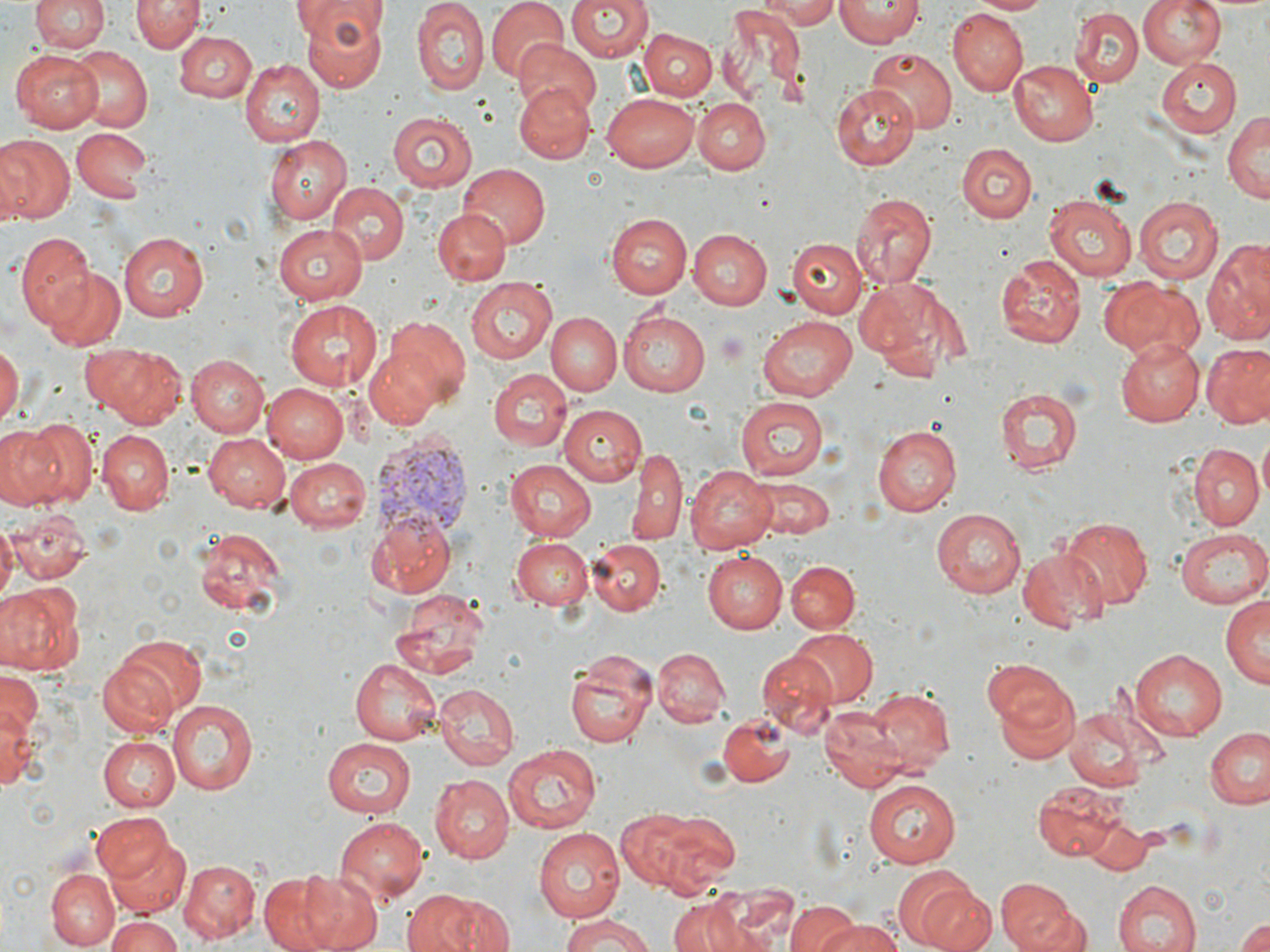

Approximate bounding boxes as (x1, y1, x2, y2) in pixels. Uninfected red blood cell locations: (31, 0, 108, 54), (133, 0, 203, 53), (294, 0, 390, 89), (487, 0, 569, 83), (566, 0, 654, 61), (756, 0, 844, 26), (835, 0, 922, 46), (967, 0, 1052, 15), (1138, 0, 1226, 68), (413, 1, 488, 96), (719, 4, 806, 99), (949, 10, 1028, 96), (1071, 10, 1142, 85), (639, 28, 717, 101), (173, 30, 257, 103), (515, 41, 604, 118), (65, 44, 153, 132), (866, 47, 957, 134), (11, 48, 105, 131), (1156, 57, 1243, 139), (238, 58, 323, 146), (1008, 58, 1097, 146), (514, 81, 595, 163), (833, 88, 918, 170), (604, 91, 702, 171), (696, 96, 771, 173), (1223, 111, 1269, 206), (388, 112, 475, 192), (71, 127, 152, 201), (0, 135, 73, 226), (264, 135, 352, 225), (959, 143, 1033, 222), (458, 164, 549, 247), (327, 181, 408, 266), (849, 192, 939, 289), (1042, 193, 1137, 283), (1133, 195, 1224, 284), (288, 197, 398, 288), (432, 209, 510, 284), (605, 213, 690, 297), (271, 222, 368, 304), (688, 229, 772, 309), (15, 232, 96, 328), (119, 232, 209, 320), (791, 237, 866, 317), (1204, 240, 1270, 345), (996, 253, 1085, 350), (44, 268, 126, 353), (465, 278, 556, 364), (860, 279, 958, 379), (1100, 280, 1203, 361), (283, 299, 384, 390), (619, 308, 714, 395), (547, 313, 619, 395), (757, 315, 861, 402), (384, 316, 470, 402), (1117, 341, 1204, 426), (1203, 342, 1270, 427), (84, 344, 187, 427), (0, 345, 21, 426), (365, 346, 444, 429), (187, 355, 269, 435), (488, 367, 571, 451), (264, 383, 349, 463), (996, 386, 1083, 477), (739, 396, 831, 478), (558, 404, 646, 486), (24, 417, 98, 508), (1, 425, 66, 510), (871, 425, 961, 516), (95, 428, 175, 515), (202, 432, 290, 511), (1188, 443, 1263, 529), (629, 446, 687, 546), (285, 458, 371, 532), (504, 459, 598, 539), (683, 464, 777, 553), (753, 480, 835, 538), (932, 508, 1026, 598), (6, 510, 90, 584), (370, 512, 458, 597), (1058, 517, 1153, 611), (0, 522, 16, 608), (1177, 526, 1270, 608), (194, 529, 288, 618), (510, 535, 593, 611), (588, 539, 666, 615), (1017, 550, 1108, 631), (705, 551, 788, 633), (786, 559, 859, 634), (0, 582, 83, 676), (391, 588, 489, 682), (1221, 593, 1269, 690), (790, 630, 876, 706), (107, 634, 209, 720), (654, 647, 729, 727), (1131, 649, 1227, 738), (564, 651, 656, 748), (759, 652, 835, 735), (98, 656, 181, 737), (351, 656, 442, 745), (983, 660, 1070, 731), (0, 670, 43, 742), (995, 680, 1083, 764), (433, 682, 517, 770), (869, 687, 954, 772), (168, 698, 259, 795), (0, 702, 41, 792), (821, 708, 905, 792), (1064, 708, 1149, 790), (718, 713, 795, 787), (1205, 726, 1270, 811), (98, 735, 178, 812), (322, 738, 417, 818), (502, 742, 604, 835), (428, 774, 513, 863), (863, 780, 962, 868), (1034, 781, 1131, 861), (631, 808, 739, 898), (92, 812, 176, 886), (333, 816, 430, 904), (1086, 817, 1152, 874), (531, 831, 624, 921), (106, 834, 192, 919), (178, 859, 258, 942), (296, 869, 383, 952), (900, 869, 996, 952), (47, 870, 118, 949), (255, 872, 355, 952), (994, 878, 1084, 952), (1110, 879, 1203, 952), (403, 887, 513, 952), (668, 897, 755, 952), (784, 900, 859, 952), (104, 914, 182, 952), (815, 915, 904, 952), (556, 916, 662, 952), (1234, 917, 1270, 952). Plasmodium vivax-infected red blood cell locations: (370, 436, 468, 547). Slide-level diagnosis: Plasmodium vivax. May-Grünwald-Giemsa stain. Image is 1270×952 pixels. Thin blood smear. 1000x magnification. Light microscopy. One field of a larger specimen.